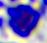 Micrograph. 400x magnification. A leukocyte is shown.